Name the parasite shown.
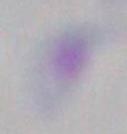
This is Toxoplasma gondii.

Micrograph. 1000x magnification.